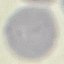 Result: no malaria parasites detected. Thin smear of blood. Photographed with a smartphone camera at the microscope eyepiece. Automatically extracted cell patch, resized to 64 × 64 pixels. Giemsa stain.